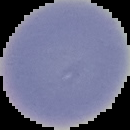
Summary:
  - Preparation: thin blood smear
  - Image size: 130×130 pixels
  - Image type: segmented cell region with the area outside set to black
  - Result: no malaria parasites detected